Outline each blood parasite and name the species.
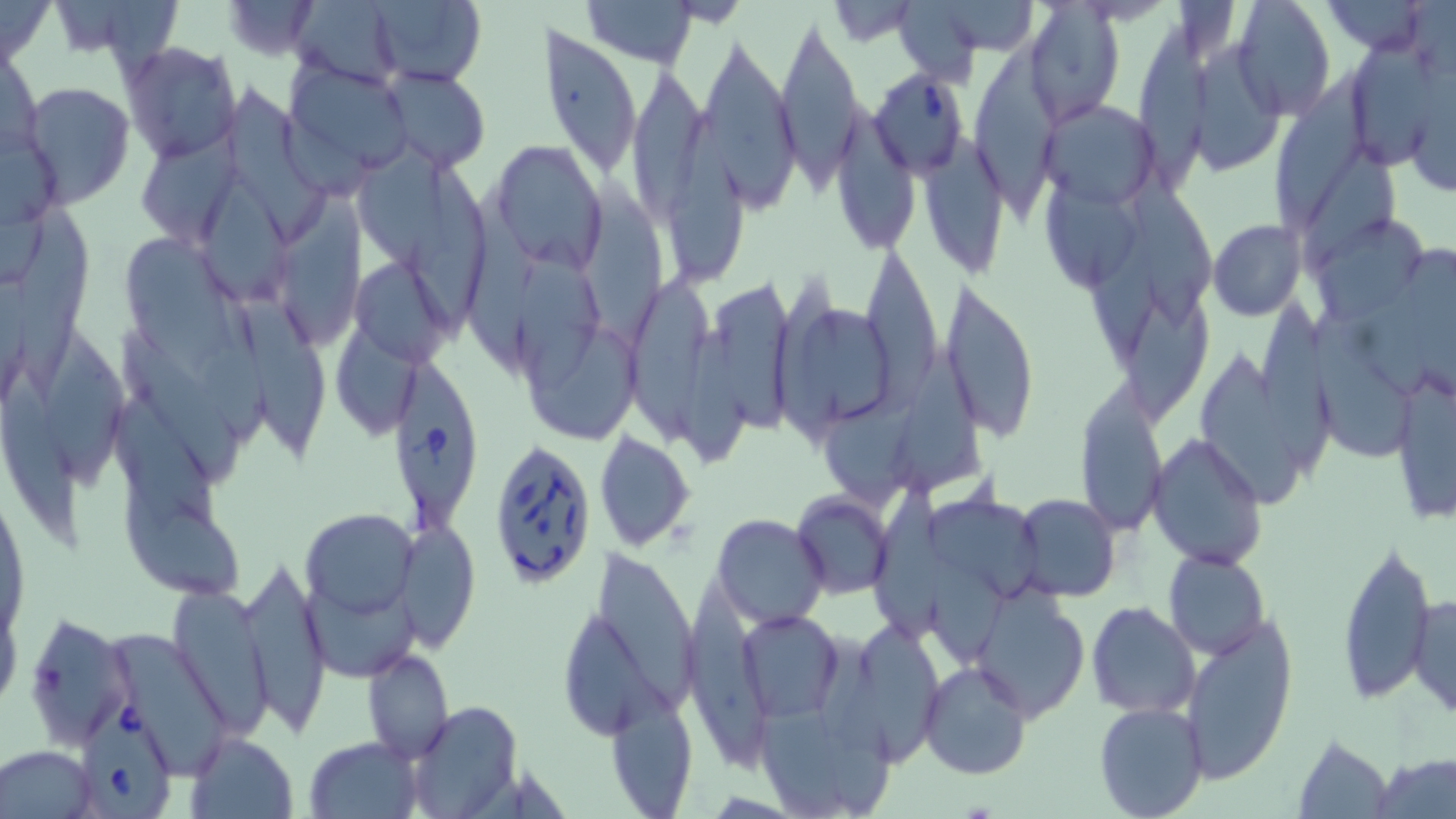

Approximate bounding boxes as [x1, y1, x2, y2] in pixels.
Babesia divergens-infected red blood cells: [871, 67, 972, 178], [395, 359, 483, 528], [484, 432, 596, 592], [90, 699, 172, 819].
No Plasmodium falciparum, Plasmodium ovale, Plasmodium malariae, Plasmodium vivax, or Trypanosoma brucei observed.

slide-level diagnosis = Babesia divergens
magnification = 1000x
preparation = thin blood film
image size = 1456×819 pixels
uninfected red blood cell locations = approximate bounding boxes as [x1, y1, x2, y2] in pixels: [0, 0, 54, 69], [223, 0, 322, 60], [290, 0, 404, 86], [368, 0, 488, 87], [578, 0, 698, 67], [900, 0, 979, 94], [1230, 0, 1335, 121], [1321, 1, 1434, 55], [928, 3, 1039, 56], [1022, 5, 1125, 126], [774, 8, 862, 187], [1136, 22, 1206, 193], [541, 25, 641, 179], [1350, 26, 1441, 175], [695, 29, 802, 216], [973, 34, 1064, 228], [1192, 36, 1283, 175], [119, 41, 242, 163], [285, 60, 414, 187], [627, 60, 712, 232], [1281, 65, 1366, 226], [50, 68, 225, 195], [378, 68, 493, 171], [21, 81, 135, 208], [226, 83, 326, 244], [1038, 100, 1161, 207], [835, 101, 919, 250], [669, 115, 753, 276], [134, 122, 243, 247], [923, 134, 1005, 274], [487, 141, 608, 272], [1305, 142, 1400, 274], [355, 144, 448, 274], [409, 151, 488, 338], [580, 161, 664, 335], [1133, 169, 1213, 324], [206, 171, 292, 309], [459, 181, 535, 374], [1044, 184, 1135, 291], [282, 189, 364, 349], [1091, 196, 1163, 372], [17, 197, 94, 393], [1315, 214, 1433, 323], [1208, 219, 1307, 321], [122, 232, 240, 375], [516, 235, 601, 395], [860, 243, 942, 384], [354, 262, 452, 361], [228, 270, 327, 453], [626, 274, 715, 443], [1125, 281, 1215, 423], [711, 282, 796, 438], [941, 282, 1038, 439], [175, 286, 270, 444], [1253, 293, 1341, 475], [778, 300, 897, 431], [1304, 314, 1417, 457], [678, 323, 747, 470], [336, 324, 411, 438], [48, 328, 123, 493], [524, 328, 641, 440], [117, 331, 247, 487], [1196, 346, 1301, 508], [891, 363, 984, 493], [1388, 364, 1455, 525], [1, 371, 85, 548], [1074, 383, 1169, 536], [805, 389, 922, 507], [117, 396, 219, 536], [593, 431, 695, 551], [1149, 433, 1268, 568], [870, 470, 949, 655], [124, 492, 245, 604], [792, 492, 895, 598], [928, 493, 1038, 600], [1013, 493, 1121, 599], [301, 506, 418, 624], [712, 514, 828, 629], [394, 518, 479, 654], [1337, 536, 1438, 706], [600, 549, 697, 707], [927, 550, 1009, 666], [1163, 550, 1270, 660], [238, 559, 332, 735], [298, 576, 420, 676], [686, 576, 775, 773], [169, 581, 276, 740], [969, 588, 1089, 722], [1408, 595, 1455, 719], [1085, 601, 1200, 718], [22, 610, 135, 747], [737, 610, 842, 720], [565, 612, 666, 735], [1178, 615, 1298, 781], [834, 616, 947, 764], [814, 629, 897, 818], [112, 631, 230, 779], [363, 647, 454, 764], [919, 661, 1032, 781], [384, 665, 498, 797], [754, 675, 846, 819], [606, 691, 699, 818], [406, 700, 524, 818], [1094, 702, 1209, 819], [185, 731, 299, 819], [1292, 733, 1394, 818], [304, 737, 423, 819], [1, 746, 99, 816], [1373, 753, 1455, 817]
modality = light microscopy
field of view = one of a larger specimen
stain = May-Grünwald-Giemsa